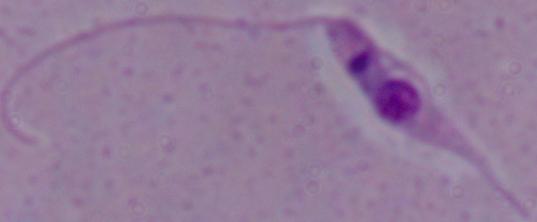

identification = Leishmania
modality = photomicrograph
magnification = 1000x